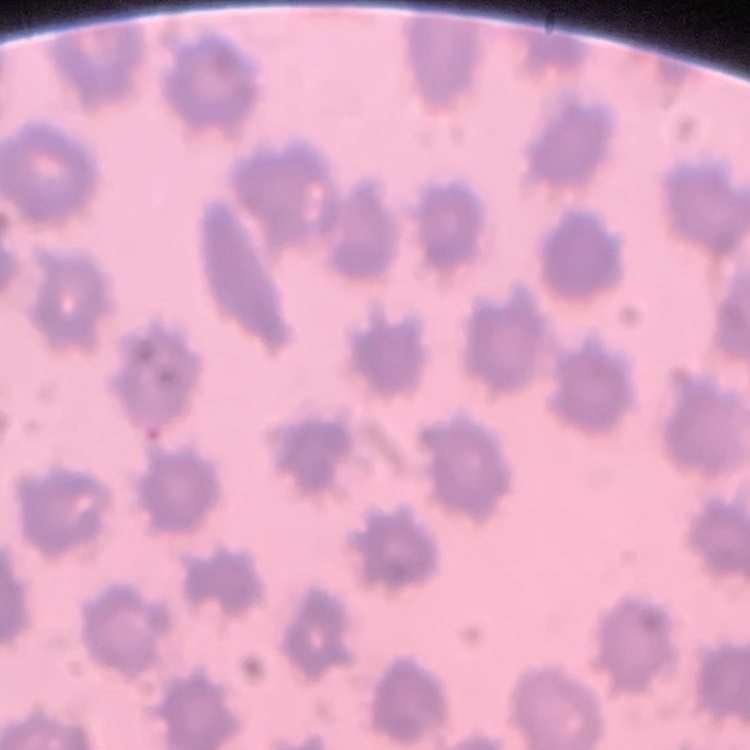
red blood cell morphology = no rouleaux formation
stain = Field's or Giemsa
image type = square crop of a larger photomicrograph
preparation = thin blood film